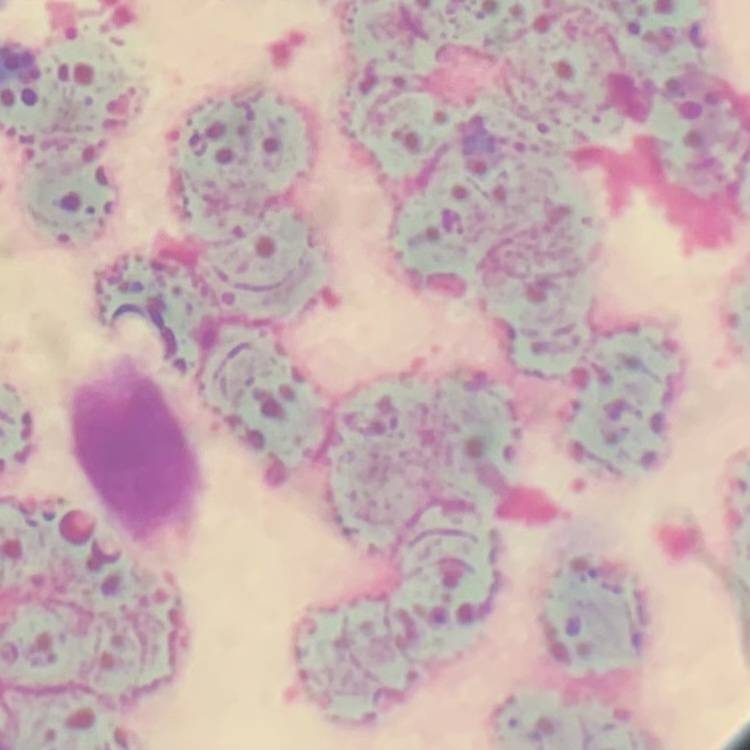
Summary:
  - Red blood cell morphology: rouleaux formation
  - Preparation: thin blood film
  - Stain: Field's or Giemsa
  - Image type: square crop of a larger photomicrograph